Assess the morphology of the erythrocytes.
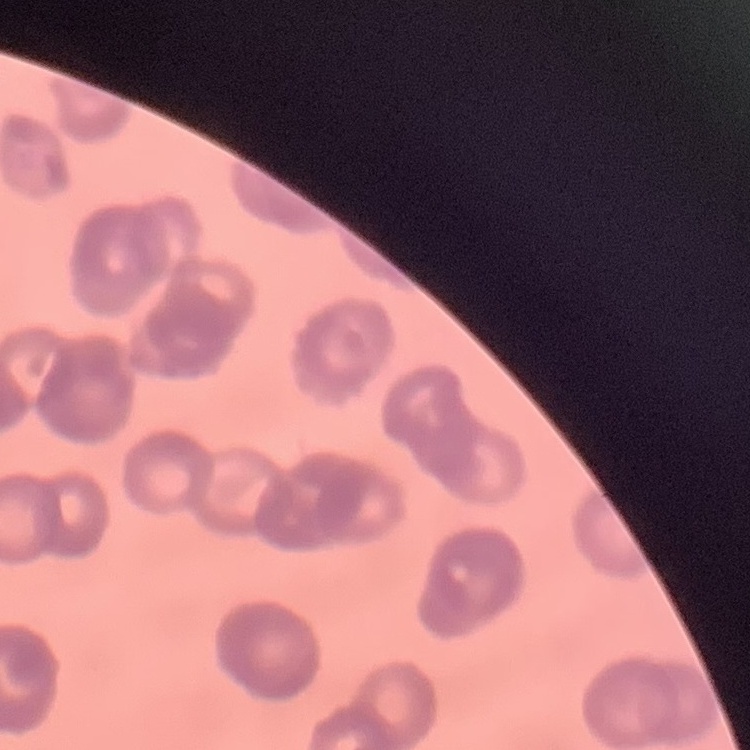

They show rouleaux formation.

Stained with either Field's or Giemsa. One tile cut from a larger photomicrograph. Thin blood smear.